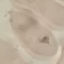
Summary:
  - Result: no malaria parasites seen
  - Preparation: thin smear
  - Image type: automatically extracted cell patch, resized to 64 × 64 pixels
  - Capture: smartphone through the microscope eyepiece
  - Stain: Giemsa